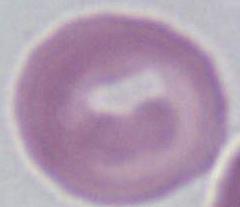
{
  "modality": "photomicrograph",
  "magnification": "1000x",
  "identification": "erythrocyte"
}